Assess this cell for malaria.
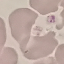
Uninfected.

capture: smartphone camera at the microscope eyepiece
stain: Giemsa
image_type: cell patch, automatically extracted from a larger field of view and resized to 64 × 64 pixels
preparation: thin blood smear